Report the malaria status of this cell.
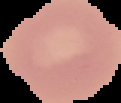
Uninfected.

From a thin blood film. Image is 121×103 pixels. The area outside the segmented cell region is set to black.